Assess the morphology of the erythrocytes.
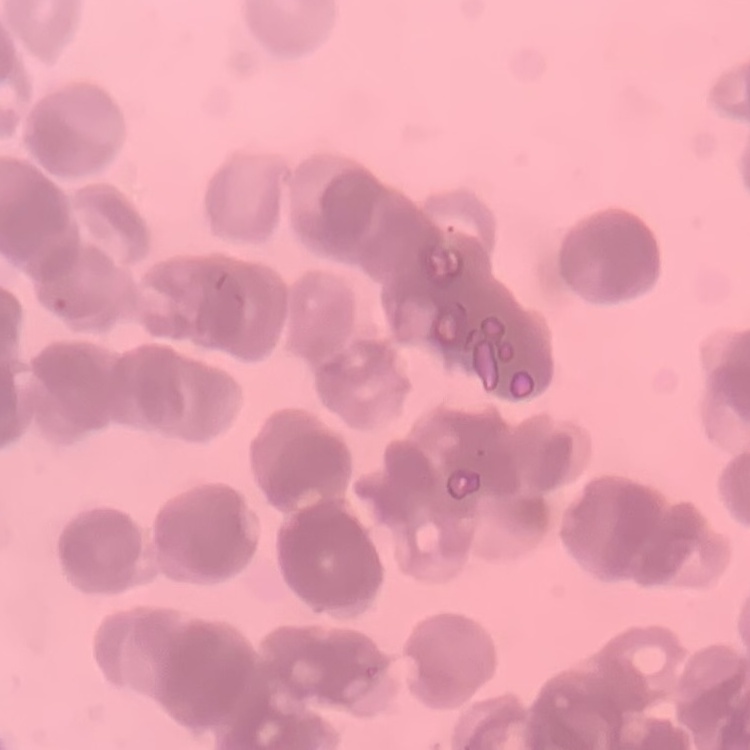
They show rouleaux formation.

Summary:
  - Stain: Field's or Giemsa
  - Image type: one tile cut from a larger photomicrograph
  - Preparation: thin blood smear